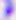
Summary:
  - Magnification: 400x
  - Identification: Toxoplasma gondii
  - Modality: micrograph